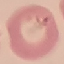

malaria status = parasitized
image type = automatically extracted cell patch, resized to 64 × 64 pixels
preparation = thin blood film
stain = Giemsa
capture = smartphone through the microscope eyepiece